Assess the morphology of the erythrocytes.
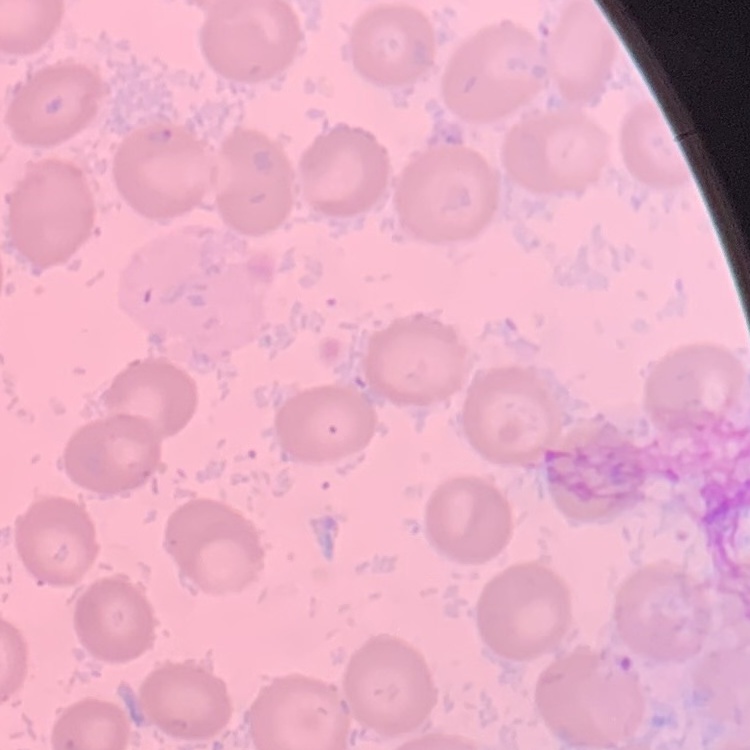
They show no rouleaux formation.

One tile cut from a larger photomicrograph. Thin peripheral smear. Field's or Giemsa stain.